Give the extent of all Plasmodium falciparum-infected red blood cells.
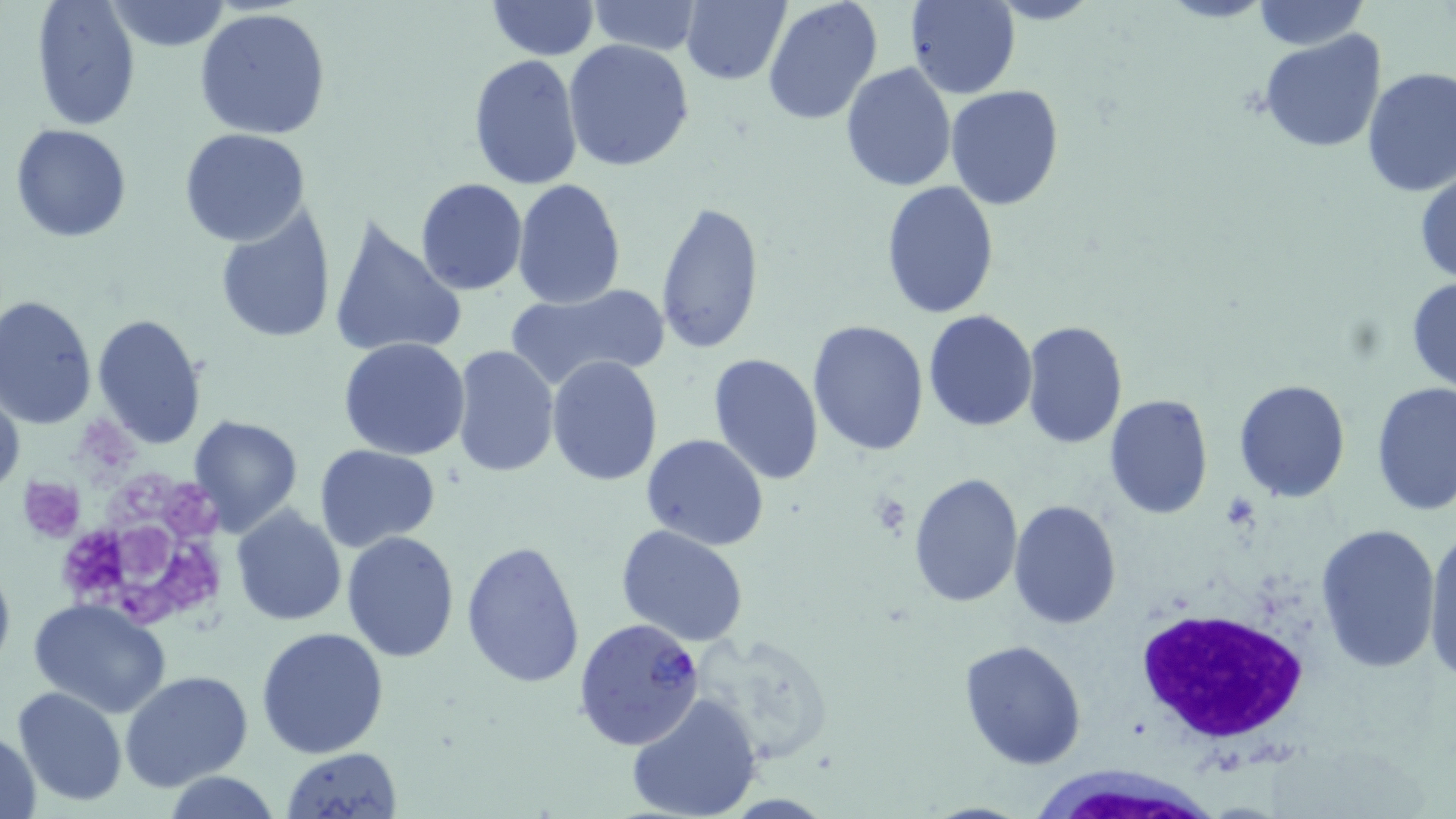
Approximate bounding boxes as (x1, y1, x2, y2) in pixels.
Plasmodium falciparum-infected red blood cells: (573, 618, 704, 746).

slide-level diagnosis = Plasmodium falciparum
magnification = 1000x
modality = optical microscopy
image size = 1456×819 pixels
preparation = thin blood smear
stain = May-Grünwald-Giemsa
field of view = one of a larger specimen
uninfected red blood cell locations = approximate bounding boxes as (x1, y1, x2, y2) in pixels: (486, 0, 598, 59), (1156, 0, 1276, 24), (31, 1, 141, 129), (103, 1, 234, 52), (586, 1, 702, 55), (681, 1, 791, 85), (904, 1, 1020, 99), (1250, 1, 1368, 49), (762, 2, 882, 125), (195, 8, 332, 139), (1256, 30, 1389, 153), (563, 40, 695, 172), (468, 54, 583, 189), (840, 63, 956, 193), (1360, 67, 1455, 196), (946, 85, 1066, 211), (10, 124, 131, 243), (179, 127, 310, 247), (1415, 168, 1456, 286), (415, 179, 526, 295), (513, 179, 626, 307), (881, 181, 1001, 321), (654, 200, 765, 354), (216, 207, 337, 345), (326, 217, 468, 361), (1406, 274, 1456, 394), (505, 282, 671, 393), (2, 294, 99, 429), (923, 309, 1039, 432), (91, 313, 208, 449), (808, 319, 929, 454), (1020, 320, 1128, 450), (339, 337, 471, 460), (451, 346, 560, 478), (708, 351, 824, 485), (546, 356, 664, 486), (1232, 377, 1353, 503), (0, 379, 24, 505), (1371, 381, 1456, 519), (1104, 394, 1213, 518), (188, 415, 302, 536), (641, 433, 768, 551), (315, 445, 439, 552), (907, 471, 1024, 607), (1008, 498, 1122, 629), (231, 507, 345, 626), (1314, 523, 1441, 673), (1422, 523, 1456, 684), (616, 524, 750, 647), (342, 530, 459, 662), (461, 539, 586, 690), (0, 553, 17, 681), (28, 599, 173, 717), (255, 627, 390, 760), (688, 630, 840, 762), (959, 639, 1088, 769), (120, 669, 253, 794), (12, 685, 126, 806), (626, 693, 760, 819), (1, 730, 44, 818), (282, 747, 401, 819), (164, 771, 283, 819)
white blood cell locations = approximate bounding boxes as (x1, y1, x2, y2) in pixels: (1131, 604, 1312, 745), (1035, 764, 1214, 819)
platelet locations = approximate bounding boxes as (x1, y1, x2, y2) in pixels: (58, 467, 233, 632), (20, 478, 84, 542), (869, 493, 912, 536)